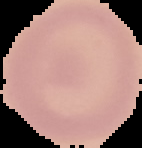
Summary:
  - Preparation: thin blood smear
  - Image type: segmented cell region on a black background
  - Result: negative for malaria parasites
  - Image size: 142×148 pixels